Assess the morphology of the erythrocytes.
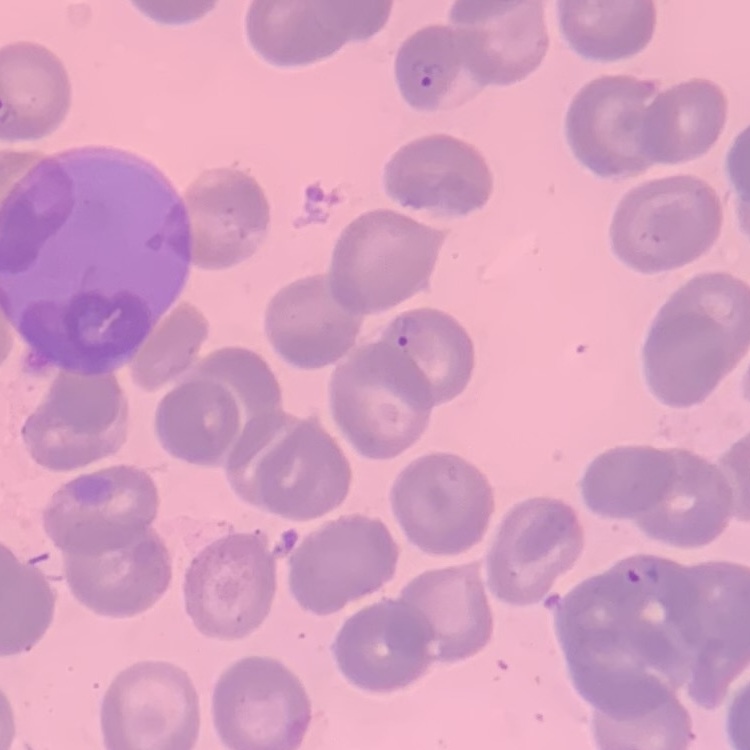

They show no rouleaux formation.

Summary:
  - Preparation: thin blood smear
  - Stain: Field's or Giemsa
  - Image type: one tile cut from a larger photomicrograph